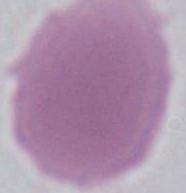 1000x magnification. Micrograph. A red blood cell is seen.